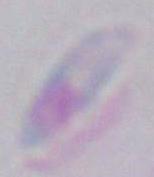
identification: Toxoplasma gondii
modality: photomicrograph
magnification: 1000x